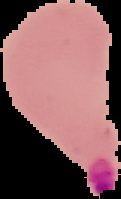

image type = segmented cell region on a black background
malaria status = parasitized
preparation = thin blood smear
image size = 121×199 pixels